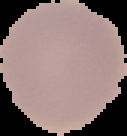

Summary:
  - Image size: 127×136 pixels
  - Preparation: thin blood smear
  - Image type: segmented cell region with the area outside set to black
  - Malaria status: uninfected